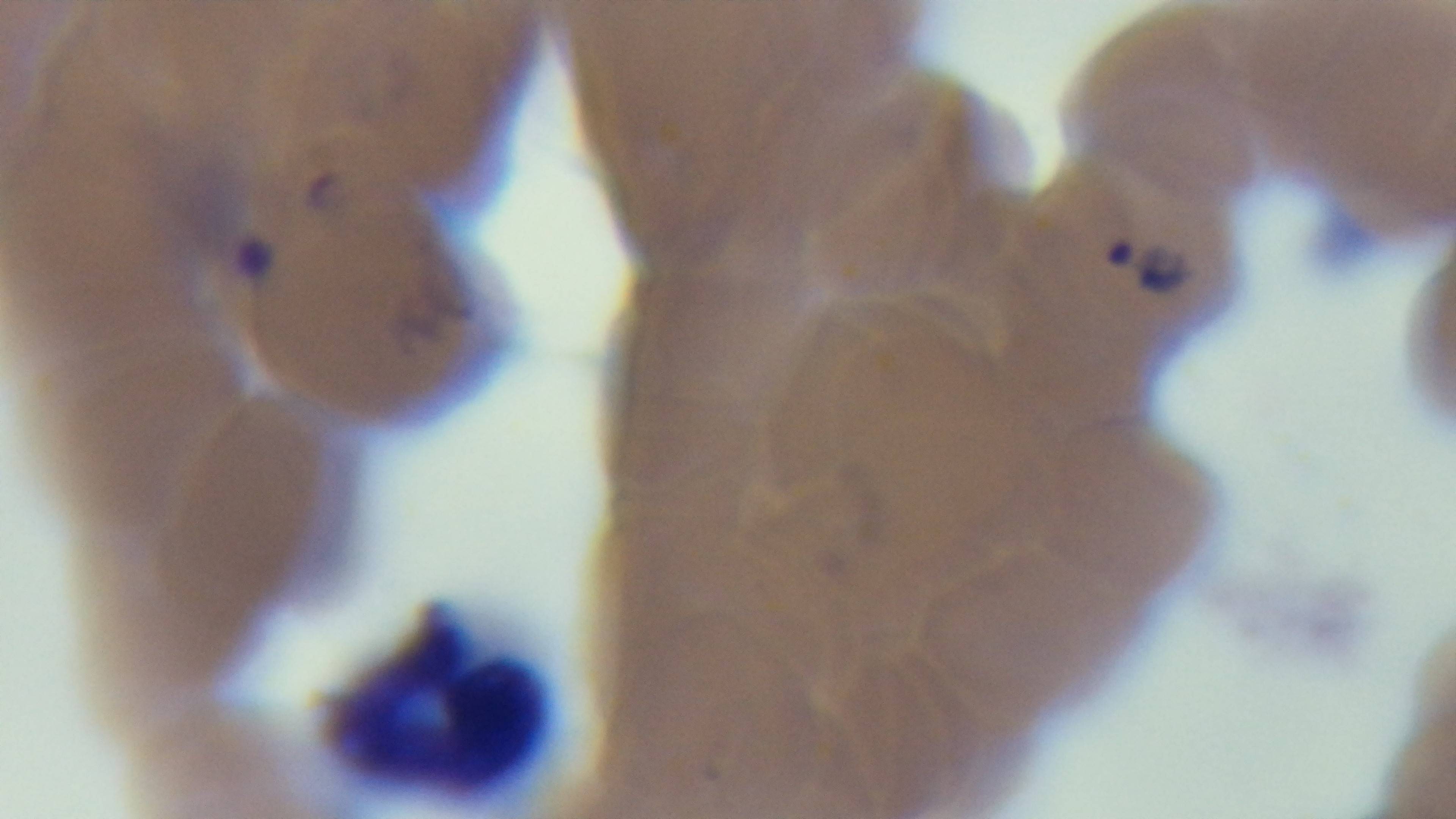

100x oil-immersion objective. Preparation: thin blood film. Giemsa stain. Captured with a mounted 4K digital camera. Malaria status: positive. Single field of view. Light microscopy.